Comment on the morphology of the red blood cells.
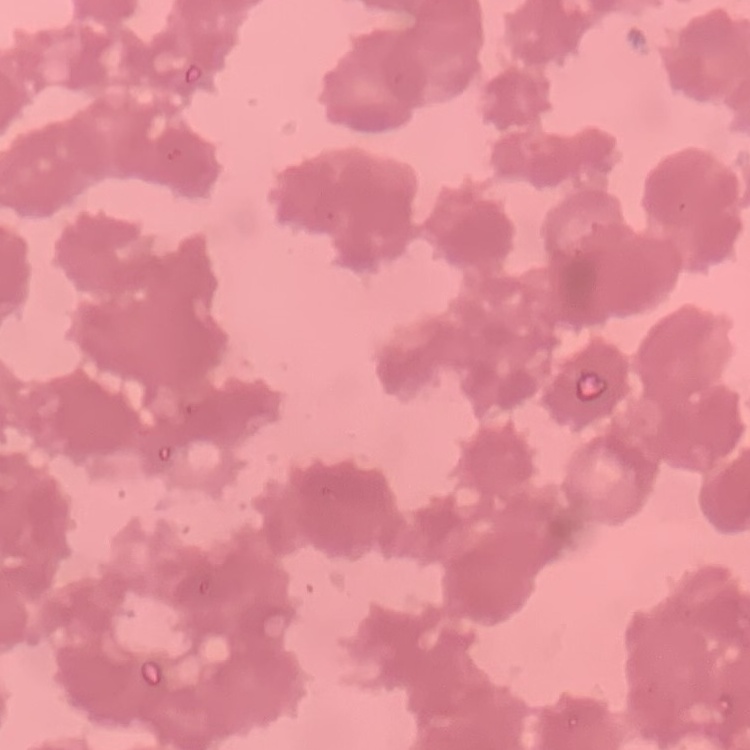
Rouleaux formation.

Stained with either Field's or Giemsa. Square crop of a larger photomicrograph. Thin blood smear.